Identify the blood parasite species.
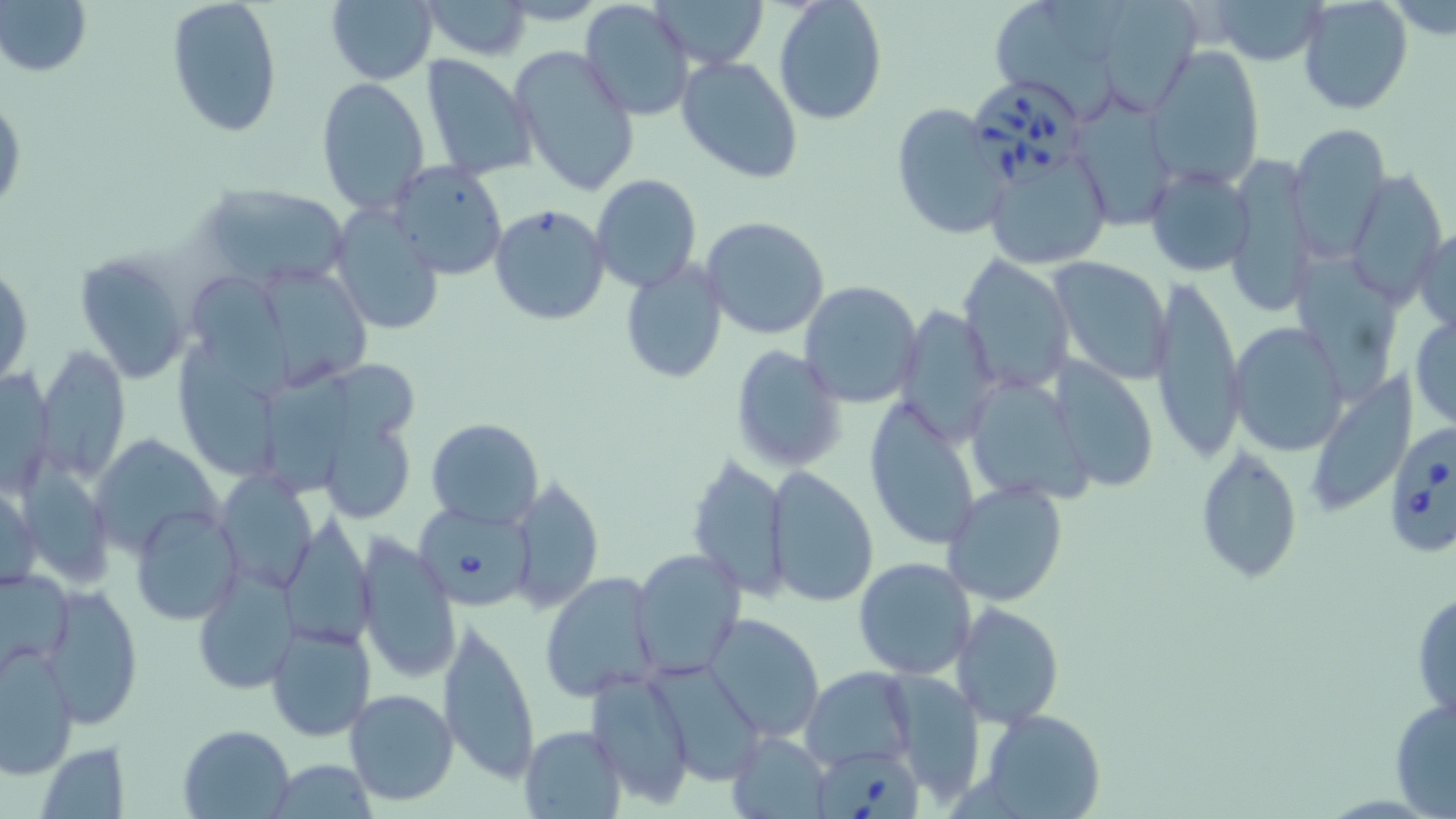
Babesia divergens.

Summary:
  - Coordinate format: approximate bounding boxes as named x1/y1/x2/y2 corners in pixels
  - Uninfected red blood cell locations: (x1=1, y1=0, x2=91, y2=79), (x1=165, y1=0, x2=283, y2=138), (x1=579, y1=0, x2=695, y2=122), (x1=652, y1=0, x2=769, y2=68), (x1=773, y1=0, x2=888, y2=123), (x1=1091, y1=0, x2=1204, y2=115), (x1=1206, y1=0, x2=1327, y2=65), (x1=1297, y1=0, x2=1414, y2=116), (x1=323, y1=1, x2=439, y2=84), (x1=421, y1=1, x2=532, y2=60), (x1=997, y1=5, x2=1125, y2=127), (x1=509, y1=45, x2=641, y2=197), (x1=1148, y1=49, x2=1263, y2=189), (x1=421, y1=53, x2=537, y2=180), (x1=676, y1=54, x2=803, y2=184), (x1=317, y1=76, x2=430, y2=213), (x1=0, y1=92, x2=25, y2=220), (x1=1072, y1=96, x2=1179, y2=230), (x1=890, y1=103, x2=1012, y2=240), (x1=1285, y1=121, x2=1391, y2=253), (x1=983, y1=146, x2=1112, y2=271), (x1=1223, y1=153, x2=1319, y2=317), (x1=390, y1=161, x2=507, y2=278), (x1=1145, y1=165, x2=1255, y2=277), (x1=1344, y1=169, x2=1445, y2=307), (x1=591, y1=175, x2=701, y2=292), (x1=201, y1=183, x2=352, y2=291), (x1=488, y1=203, x2=611, y2=325), (x1=330, y1=204, x2=445, y2=337), (x1=700, y1=216, x2=831, y2=341), (x1=1413, y1=223, x2=1456, y2=336), (x1=72, y1=249, x2=194, y2=385), (x1=1296, y1=252, x2=1397, y2=398), (x1=956, y1=254, x2=1076, y2=394), (x1=1048, y1=254, x2=1172, y2=384), (x1=619, y1=259, x2=730, y2=385), (x1=1, y1=261, x2=33, y2=390), (x1=258, y1=272, x2=377, y2=383), (x1=189, y1=273, x2=299, y2=403), (x1=1149, y1=277, x2=1244, y2=464), (x1=798, y1=280, x2=922, y2=409), (x1=895, y1=304, x2=999, y2=448), (x1=1409, y1=312, x2=1456, y2=429), (x1=1229, y1=321, x2=1349, y2=457), (x1=731, y1=344, x2=844, y2=472), (x1=173, y1=345, x2=280, y2=480), (x1=34, y1=348, x2=130, y2=483), (x1=1048, y1=358, x2=1161, y2=494), (x1=1, y1=364, x2=56, y2=498), (x1=262, y1=364, x2=352, y2=496), (x1=1303, y1=370, x2=1420, y2=518), (x1=963, y1=375, x2=1093, y2=505), (x1=865, y1=394, x2=983, y2=550), (x1=324, y1=402, x2=419, y2=527), (x1=426, y1=418, x2=543, y2=528), (x1=92, y1=435, x2=221, y2=557), (x1=1194, y1=442, x2=1302, y2=586), (x1=685, y1=455, x2=789, y2=601), (x1=765, y1=466, x2=879, y2=608), (x1=212, y1=470, x2=318, y2=593), (x1=507, y1=474, x2=604, y2=614), (x1=0, y1=477, x2=41, y2=595), (x1=942, y1=480, x2=1069, y2=607), (x1=130, y1=505, x2=242, y2=625), (x1=279, y1=514, x2=378, y2=650), (x1=355, y1=534, x2=461, y2=684), (x1=629, y1=548, x2=746, y2=677), (x1=852, y1=556, x2=977, y2=680), (x1=193, y1=563, x2=299, y2=697), (x1=0, y1=566, x2=75, y2=671), (x1=538, y1=572, x2=665, y2=703), (x1=40, y1=582, x2=142, y2=727), (x1=1412, y1=586, x2=1455, y2=727), (x1=952, y1=600, x2=1064, y2=728), (x1=438, y1=613, x2=541, y2=789), (x1=704, y1=613, x2=824, y2=741), (x1=266, y1=621, x2=376, y2=740), (x1=0, y1=642, x2=78, y2=778), (x1=802, y1=667, x2=919, y2=771), (x1=588, y1=669, x2=698, y2=809), (x1=883, y1=671, x2=988, y2=804), (x1=342, y1=688, x2=458, y2=806), (x1=1389, y1=695, x2=1456, y2=817), (x1=977, y1=708, x2=1108, y2=819), (x1=178, y1=724, x2=296, y2=817), (x1=519, y1=725, x2=626, y2=818), (x1=726, y1=732, x2=831, y2=816), (x1=37, y1=740, x2=129, y2=816), (x1=262, y1=761, x2=380, y2=817)
  - Babesia divergens-infected red blood cell locations: (x1=973, y1=79, x2=1083, y2=193), (x1=1382, y1=423, x2=1456, y2=560), (x1=416, y1=508, x2=536, y2=613), (x1=807, y1=742, x2=925, y2=818)
  - Stain: May-Grünwald-Giemsa
  - Modality: optical microscopy
  - Preparation: thin blood smear
  - Magnification: 1000x
  - Field of view: one of a larger specimen
  - Image size: 1456×819 pixels